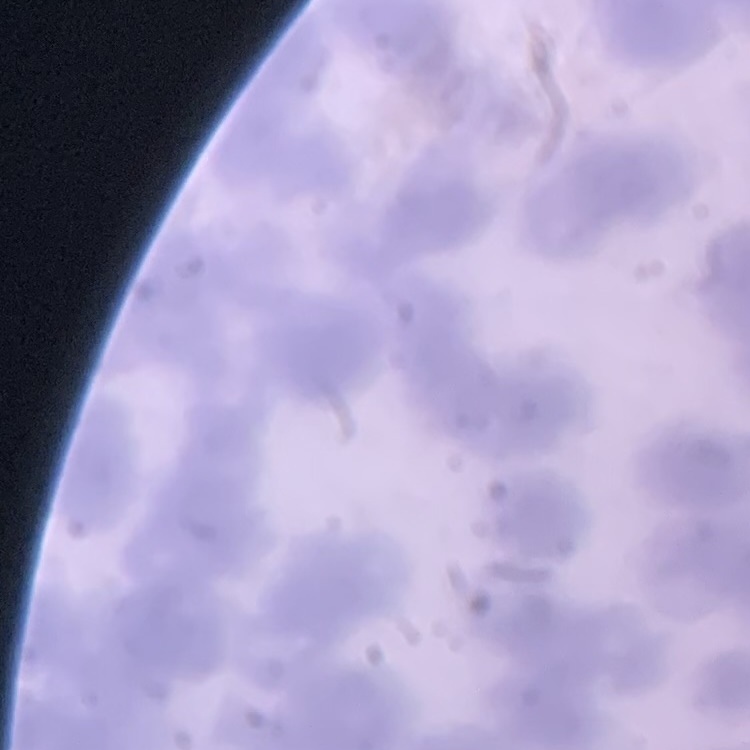

Summary:
  - Red blood cell morphology: rouleaux formation
  - Stain: Field's or Giemsa
  - Preparation: thin blood film
  - Image type: one tile cut from a larger photomicrograph